Identify the blood parasite species.
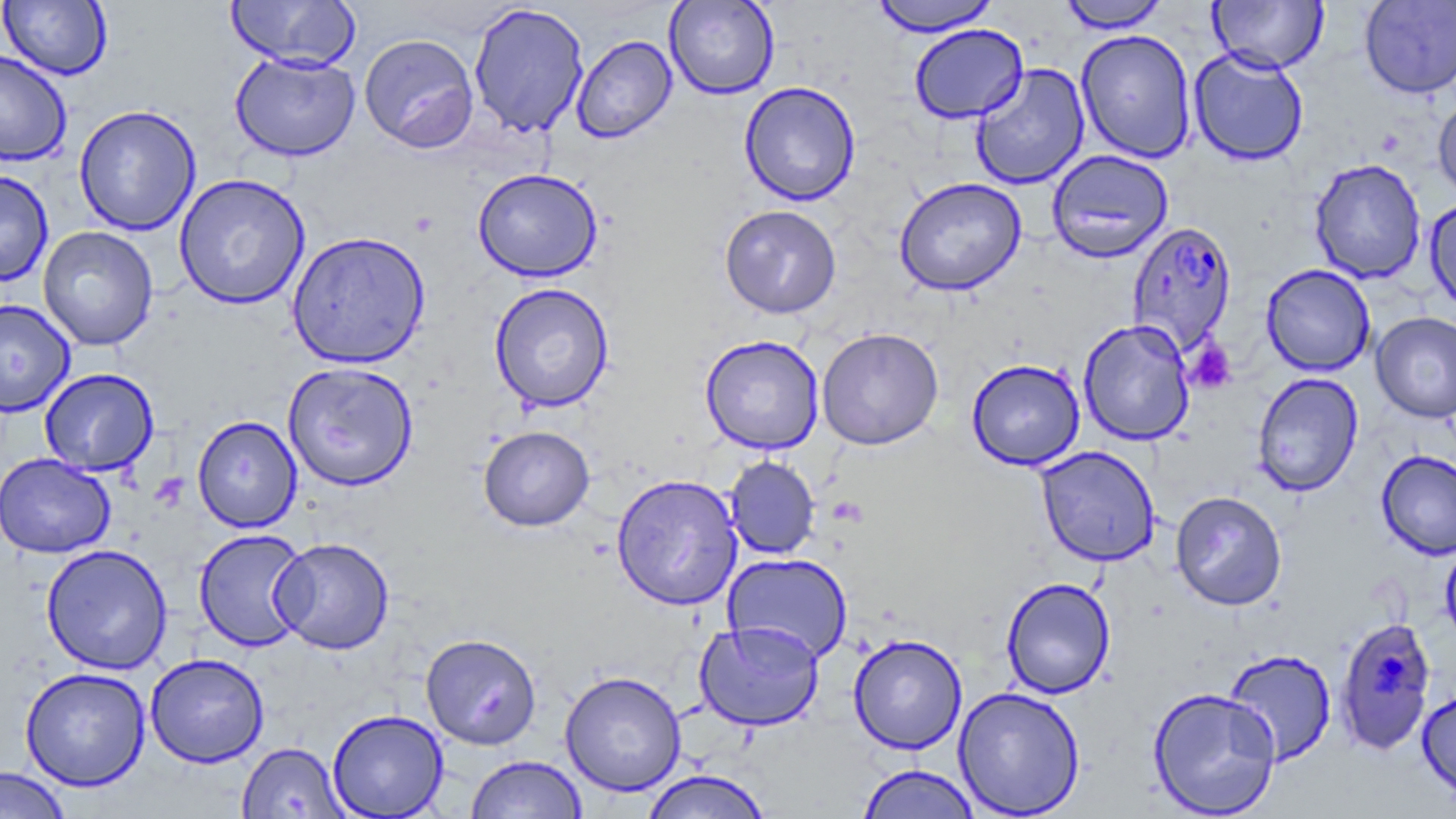
Plasmodium falciparum.

Summary:
  - Coordinate format: approximate bounding boxes as named x1/y1/x2/y2 corners in pixels
  - Uninfected red blood cell locations (subset): (x1=0, y1=0, x2=112, y2=81), (x1=226, y1=0, x2=360, y2=70), (x1=664, y1=0, x2=780, y2=99), (x1=870, y1=0, x2=1000, y2=36), (x1=1057, y1=0, x2=1171, y2=33), (x1=1209, y1=0, x2=1328, y2=73), (x1=1359, y1=1, x2=1456, y2=99), (x1=468, y1=3, x2=590, y2=137), (x1=908, y1=24, x2=1028, y2=123), (x1=1076, y1=28, x2=1197, y2=164), (x1=359, y1=33, x2=479, y2=153), (x1=571, y1=35, x2=677, y2=144), (x1=1189, y1=47, x2=1309, y2=166), (x1=0, y1=49, x2=72, y2=166), (x1=230, y1=51, x2=360, y2=162), (x1=970, y1=63, x2=1090, y2=190), (x1=738, y1=81, x2=861, y2=206), (x1=1432, y1=94, x2=1456, y2=202), (x1=74, y1=105, x2=201, y2=235), (x1=1047, y1=149, x2=1174, y2=263), (x1=1309, y1=158, x2=1426, y2=283), (x1=472, y1=168, x2=603, y2=282), (x1=0, y1=170, x2=54, y2=287), (x1=173, y1=173, x2=310, y2=310), (x1=894, y1=177, x2=1027, y2=296), (x1=1424, y1=196, x2=1456, y2=316), (x1=719, y1=204, x2=842, y2=318), (x1=38, y1=226, x2=158, y2=351), (x1=287, y1=231, x2=431, y2=369), (x1=1261, y1=264, x2=1376, y2=376), (x1=489, y1=282, x2=615, y2=413), (x1=0, y1=298, x2=75, y2=417), (x1=1371, y1=311, x2=1456, y2=423), (x1=1078, y1=320, x2=1195, y2=446), (x1=816, y1=328, x2=944, y2=450), (x1=700, y1=335, x2=824, y2=454), (x1=966, y1=358, x2=1085, y2=470), (x1=282, y1=361, x2=419, y2=492), (x1=39, y1=368, x2=159, y2=476), (x1=1252, y1=372, x2=1363, y2=497), (x1=192, y1=415, x2=302, y2=533), (x1=478, y1=425, x2=594, y2=531), (x1=1035, y1=445, x2=1161, y2=566), (x1=1376, y1=450, x2=1456, y2=561), (x1=0, y1=452, x2=115, y2=558), (x1=724, y1=456, x2=820, y2=560), (x1=611, y1=473, x2=744, y2=611), (x1=1170, y1=490, x2=1287, y2=610), (x1=193, y1=528, x2=311, y2=652), (x1=271, y1=537, x2=395, y2=654), (x1=1440, y1=539, x2=1456, y2=648), (x1=41, y1=544, x2=172, y2=674), (x1=722, y1=552, x2=853, y2=663), (x1=1001, y1=577, x2=1116, y2=699), (x1=694, y1=620, x2=825, y2=731), (x1=421, y1=633, x2=542, y2=750), (x1=848, y1=633, x2=967, y2=753), (x1=1224, y1=648, x2=1337, y2=765), (x1=145, y1=653, x2=269, y2=768), (x1=20, y1=667, x2=151, y2=791), (x1=560, y1=670, x2=687, y2=796), (x1=953, y1=686, x2=1086, y2=818), (x1=1148, y1=687, x2=1282, y2=818), (x1=1417, y1=689, x2=1456, y2=804), (x1=327, y1=709, x2=449, y2=818), (x1=236, y1=741, x2=350, y2=818), (x1=465, y1=754, x2=587, y2=818), (x1=856, y1=763, x2=982, y2=819), (x1=0, y1=766, x2=72, y2=818), (x1=642, y1=769, x2=772, y2=819)
  - Platelet locations: (x1=1184, y1=339, x2=1237, y2=394), (x1=827, y1=496, x2=867, y2=526)
  - Plasmodium falciparum-infected red blood cell locations (subset): (x1=1125, y1=221, x2=1238, y2=354)
  - Preparation: thin blood smear
  - Stain: May-Grünwald-Giemsa
  - Image size: 1456×819 pixels
  - Modality: light microscopy
  - Magnification: 1000x
  - Field of view: one of a larger specimen